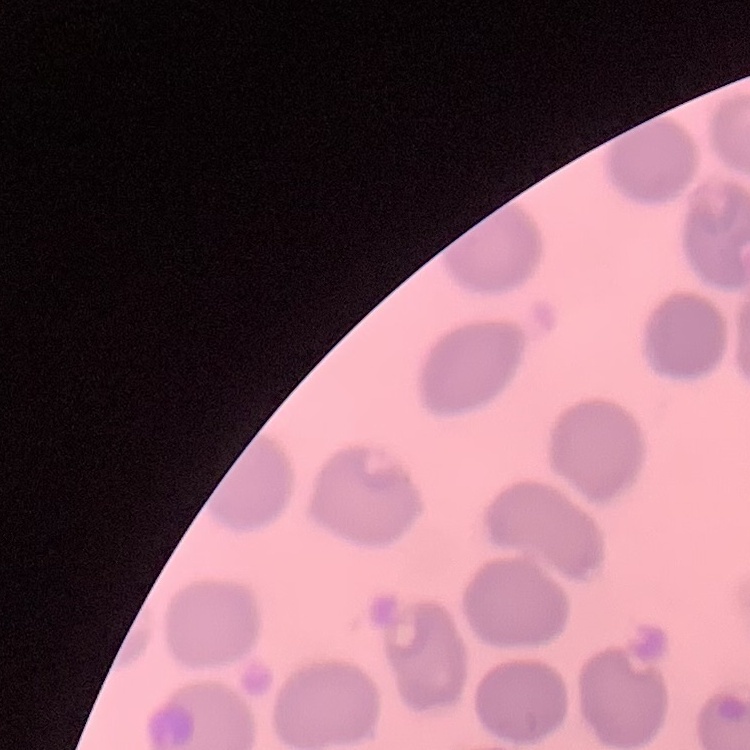
Summary:
  - Erythrocyte morphology: no rouleaux formation
  - Stain: Field's or Giemsa
  - Preparation: thin peripheral smear
  - Image type: one tile cut from a larger photomicrograph